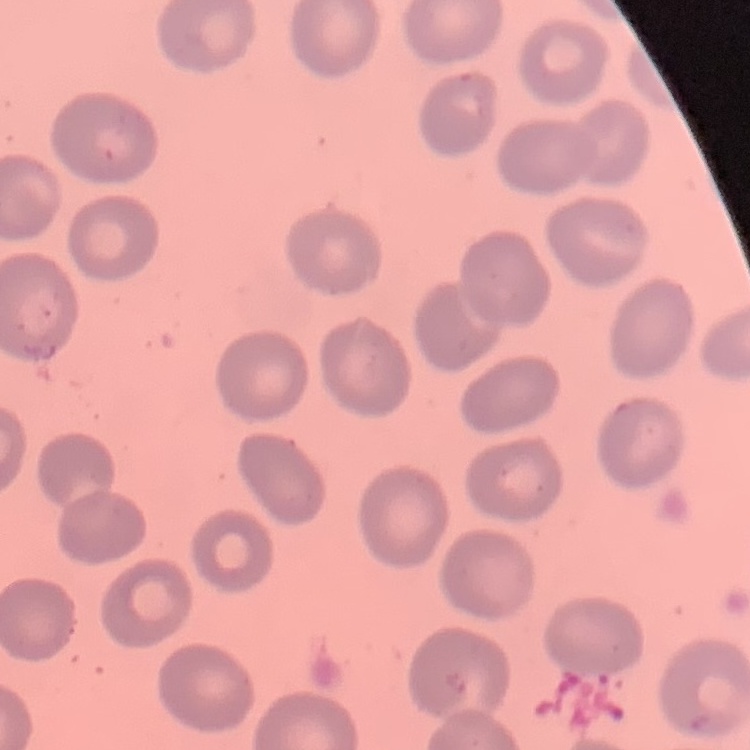

red blood cell morphology = no rouleaux formation
stain = Field's or Giemsa
preparation = thin blood film
image type = square crop of a larger photomicrograph